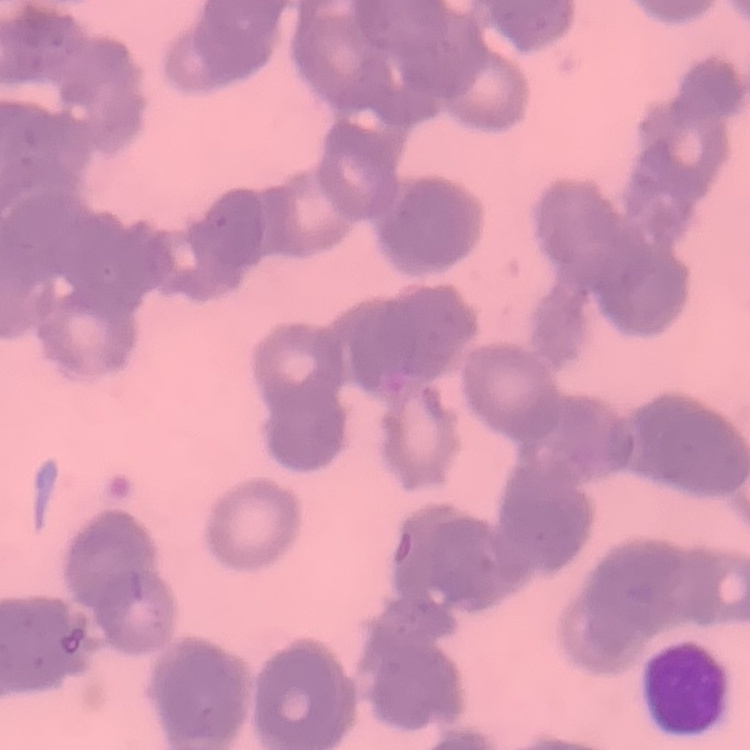

The erythrocytes show rouleaux formation. Stained with either Field's or Giemsa. One tile cut from a larger photomicrograph. Thin blood film.